Locate and identify every blood parasite.
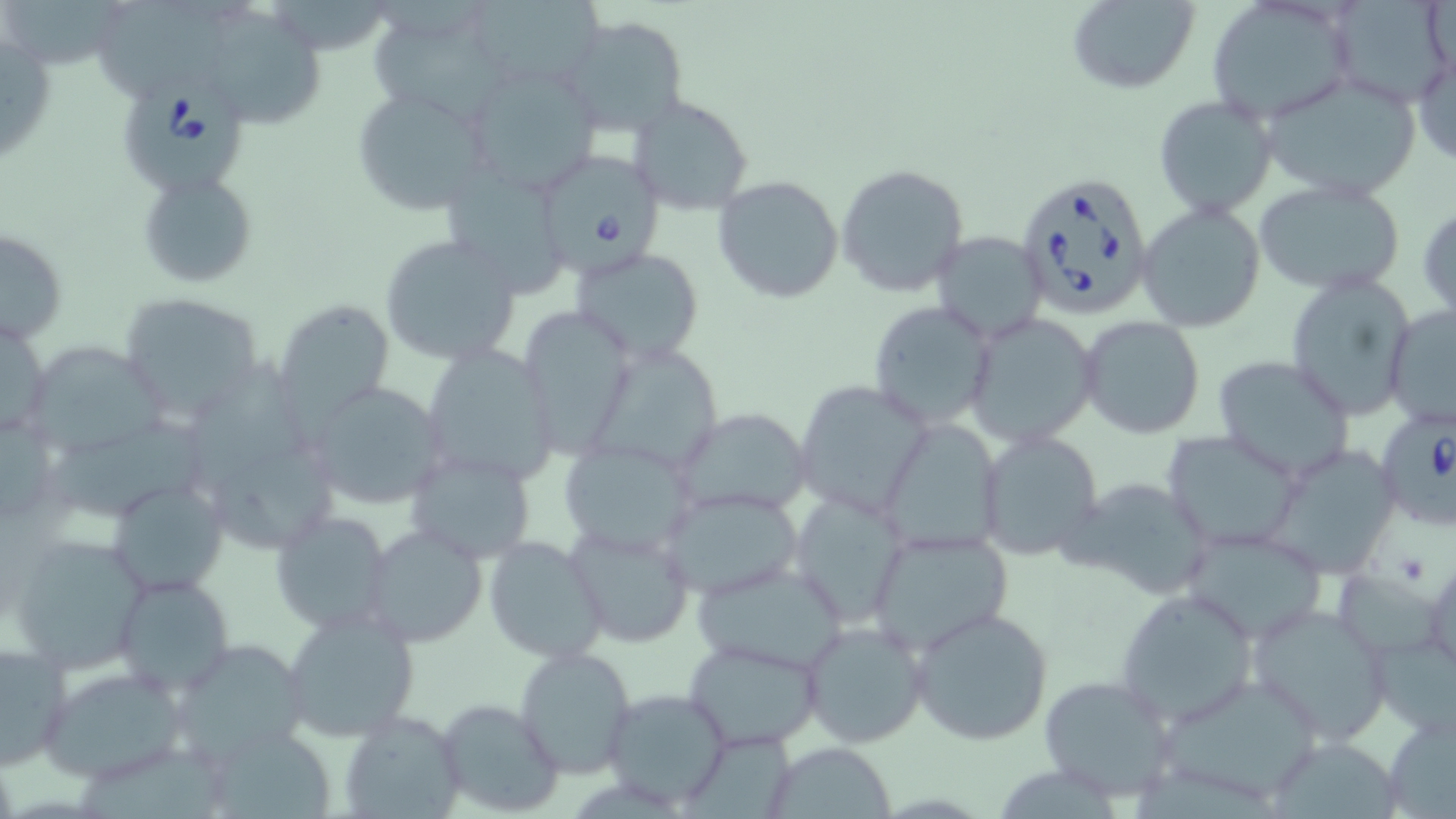

Approximate bounding boxes as (x1, y1, x2, y2) in pixels.
Babesia divergens-infected red blood cells: (123, 82, 252, 192), (530, 147, 666, 273), (1012, 173, 1155, 319), (1373, 406, 1455, 529).
No Plasmodium falciparum, Plasmodium ovale, Plasmodium malariae, Plasmodium vivax, or Trypanosoma brucei observed.

slide-level diagnosis = Babesia divergens
field of view = one of a larger specimen
stain = May-Grünwald-Giemsa
image size = 1456×819 pixels
preparation = thin blood smear
uninfected red blood cell locations = approximate bounding boxes as (x1, y1, x2, y2) in pixels: (466, 0, 604, 90), (1066, 0, 1201, 94), (1204, 0, 1359, 125), (1329, 0, 1455, 110), (99, 1, 233, 106), (366, 1, 516, 122), (1, 2, 126, 69), (200, 7, 324, 127), (558, 15, 689, 137), (0, 29, 58, 171), (1412, 36, 1455, 170), (460, 61, 602, 202), (1256, 72, 1422, 202), (352, 85, 495, 217), (1153, 94, 1277, 218), (630, 95, 754, 215), (834, 162, 970, 298), (138, 169, 259, 289), (713, 175, 845, 304), (1251, 179, 1407, 297), (1419, 198, 1456, 326), (1136, 203, 1266, 334), (1, 228, 69, 346), (930, 230, 1050, 343), (378, 233, 521, 366), (571, 248, 704, 365), (1284, 272, 1416, 420), (116, 291, 265, 419), (272, 298, 396, 426), (865, 300, 996, 429), (1383, 304, 1456, 429), (517, 309, 636, 458), (965, 313, 1100, 448), (0, 315, 49, 443), (1078, 315, 1206, 438), (420, 343, 559, 490), (20, 344, 174, 460), (183, 349, 310, 499), (593, 349, 720, 465), (1210, 355, 1356, 481), (305, 379, 448, 510), (793, 379, 932, 518), (670, 406, 814, 519), (0, 409, 58, 533), (54, 418, 208, 522), (877, 418, 1006, 555), (976, 427, 1103, 561), (1163, 431, 1302, 551), (555, 438, 701, 558), (404, 449, 537, 565), (1270, 453, 1396, 580), (206, 459, 340, 557), (1062, 473, 1216, 600), (107, 476, 231, 597), (659, 487, 808, 601), (788, 491, 909, 627), (270, 507, 396, 633), (563, 519, 697, 647), (360, 522, 488, 647), (864, 526, 1014, 657), (1180, 527, 1332, 643), (5, 532, 149, 675), (482, 536, 608, 664), (1424, 555, 1456, 682), (691, 557, 850, 675), (111, 574, 236, 696), (1115, 587, 1259, 727), (1245, 601, 1395, 743), (280, 605, 422, 744), (909, 605, 1055, 746), (799, 619, 930, 749), (172, 636, 308, 764), (681, 636, 826, 749), (1375, 637, 1456, 731), (0, 642, 73, 773), (513, 645, 636, 776), (40, 664, 191, 783), (1039, 672, 1179, 804), (1163, 674, 1318, 791), (601, 687, 734, 809), (435, 697, 564, 818), (1380, 705, 1456, 817), (339, 709, 467, 818), (205, 723, 336, 819), (684, 733, 798, 819), (763, 742, 897, 817), (1272, 744, 1397, 819)
magnification = 1000x
modality = optical microscopy